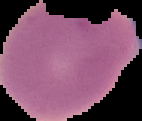

malaria_status: uninfected
preparation: thin blood smear
image_type: segmented cell region with the area outside set to black
image_size: 142×121 pixels